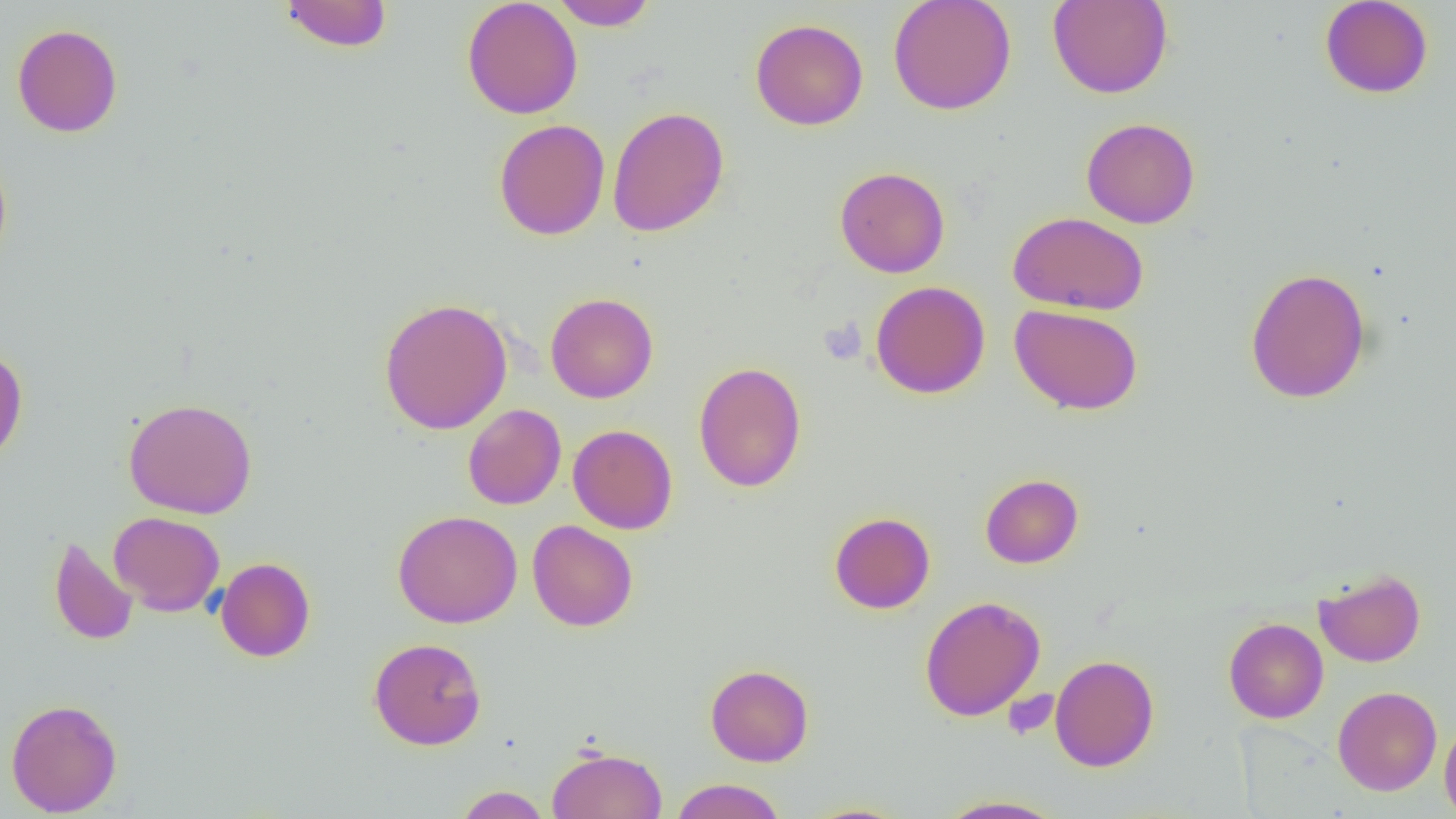

Approximate bounding boxes as (x1, y1, x2, y2) in pixels. Platelet locations: (820, 319, 867, 365). Uninfected red blood cell locations: (279, 0, 394, 53), (462, 0, 583, 119), (550, 0, 658, 31), (887, 0, 1016, 115), (1047, 0, 1173, 99), (1319, 0, 1434, 99), (750, 18, 868, 130), (11, 24, 123, 138), (607, 105, 729, 237), (1081, 117, 1200, 228), (494, 119, 610, 240), (0, 151, 13, 271), (834, 166, 950, 278), (1008, 211, 1148, 315), (1245, 267, 1371, 403), (870, 281, 990, 399), (545, 292, 658, 403), (378, 297, 513, 435), (1009, 303, 1144, 415), (0, 346, 28, 465), (693, 361, 807, 493), (123, 397, 257, 519), (463, 404, 566, 510), (568, 424, 678, 534), (980, 474, 1083, 568), (392, 509, 522, 629), (109, 511, 225, 616), (829, 512, 935, 614), (526, 520, 638, 632), (48, 535, 138, 646), (215, 557, 316, 662), (1314, 569, 1425, 667), (919, 595, 1045, 721), (1223, 617, 1328, 723), (368, 637, 487, 750), (1049, 654, 1159, 771), (705, 664, 814, 766), (1332, 686, 1442, 796), (5, 698, 122, 816), (1440, 716, 1456, 819), (547, 745, 668, 819), (669, 778, 787, 819), (453, 785, 552, 819), (934, 794, 1070, 818). Slide-level diagnosis: no evidence of blood parasites. Thin blood film. Image is 1456×819 pixels. 1000x magnification. Light microscopy. One field of a larger specimen.